Locate and identify every blood parasite.
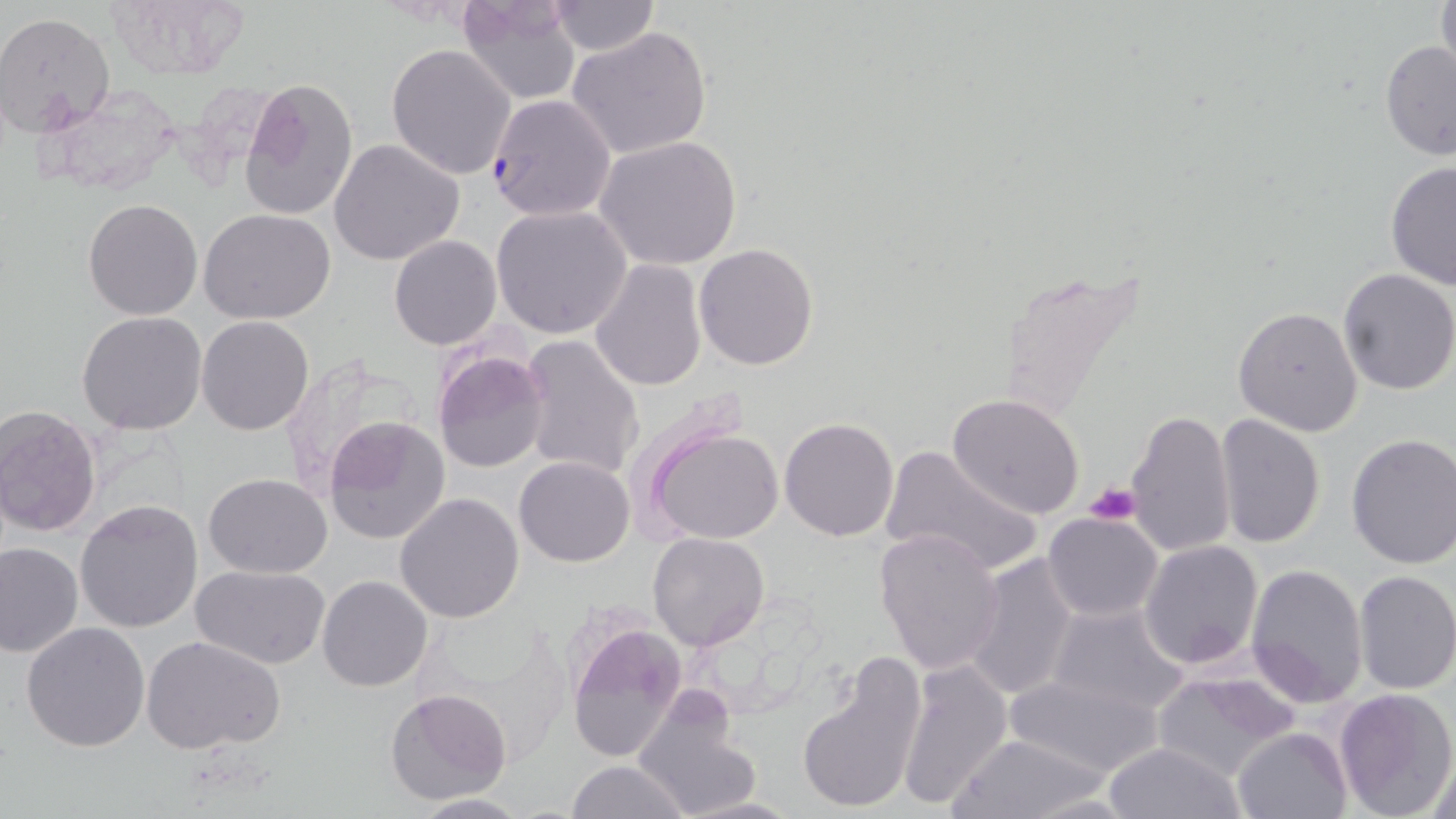
Approximate bounding boxes as named x1/y1/x2/y2 corners in pixels.
Plasmodium falciparum-infected red blood cells: (x1=486, y1=93, x2=617, y2=223).
No Plasmodium ovale, Plasmodium malariae, Plasmodium vivax, Babesia divergens, or Trypanosoma brucei observed.

Summary:
  - Platelet locations: (x1=1085, y1=483, x2=1142, y2=526)
  - Uninfected red blood cell locations: (x1=455, y1=0, x2=582, y2=105), (x1=1433, y1=0, x2=1455, y2=82), (x1=103, y1=1, x2=249, y2=81), (x1=547, y1=1, x2=660, y2=55), (x1=0, y1=13, x2=115, y2=137), (x1=567, y1=24, x2=714, y2=160), (x1=1379, y1=39, x2=1456, y2=160), (x1=386, y1=42, x2=516, y2=179), (x1=239, y1=75, x2=359, y2=223), (x1=594, y1=136, x2=743, y2=270), (x1=328, y1=139, x2=464, y2=267), (x1=1383, y1=159, x2=1456, y2=291), (x1=81, y1=199, x2=202, y2=320), (x1=489, y1=204, x2=632, y2=340), (x1=198, y1=209, x2=337, y2=325), (x1=389, y1=235, x2=501, y2=349), (x1=693, y1=243, x2=818, y2=370), (x1=591, y1=259, x2=708, y2=392), (x1=990, y1=267, x2=1153, y2=426), (x1=1336, y1=268, x2=1456, y2=395), (x1=1232, y1=306, x2=1364, y2=434), (x1=76, y1=311, x2=207, y2=434), (x1=196, y1=315, x2=315, y2=436), (x1=518, y1=334, x2=645, y2=481), (x1=432, y1=347, x2=550, y2=472), (x1=947, y1=394, x2=1086, y2=519), (x1=0, y1=406, x2=102, y2=539), (x1=1125, y1=409, x2=1236, y2=556), (x1=1214, y1=412, x2=1325, y2=550), (x1=323, y1=417, x2=451, y2=544), (x1=778, y1=418, x2=900, y2=541), (x1=645, y1=422, x2=786, y2=546), (x1=1345, y1=433, x2=1456, y2=569), (x1=879, y1=444, x2=1043, y2=580), (x1=514, y1=455, x2=634, y2=567), (x1=204, y1=473, x2=330, y2=577), (x1=394, y1=493, x2=523, y2=624), (x1=74, y1=498, x2=204, y2=633), (x1=1042, y1=511, x2=1163, y2=622), (x1=872, y1=528, x2=1005, y2=673), (x1=648, y1=532, x2=769, y2=651), (x1=1139, y1=540, x2=1262, y2=669), (x1=0, y1=542, x2=83, y2=659), (x1=963, y1=552, x2=1080, y2=701), (x1=192, y1=564, x2=331, y2=669), (x1=1244, y1=564, x2=1366, y2=708), (x1=1354, y1=570, x2=1456, y2=695), (x1=317, y1=575, x2=433, y2=692), (x1=1045, y1=600, x2=1191, y2=714), (x1=562, y1=619, x2=688, y2=765), (x1=22, y1=623, x2=151, y2=752), (x1=142, y1=636, x2=287, y2=754), (x1=795, y1=655, x2=926, y2=816), (x1=897, y1=659, x2=1012, y2=807), (x1=1004, y1=672, x2=1165, y2=777), (x1=1152, y1=672, x2=1300, y2=781), (x1=1334, y1=686, x2=1456, y2=818), (x1=385, y1=689, x2=511, y2=806), (x1=633, y1=696, x2=763, y2=818), (x1=1232, y1=727, x2=1351, y2=818), (x1=946, y1=733, x2=1112, y2=819), (x1=1101, y1=741, x2=1247, y2=819), (x1=1427, y1=748, x2=1455, y2=819), (x1=566, y1=760, x2=690, y2=819), (x1=407, y1=793, x2=530, y2=817), (x1=677, y1=794, x2=804, y2=818)
  - Slide-level diagnosis: Plasmodium falciparum
  - Image size: 1456×819 pixels
  - Field of view: single
  - Preparation: thin blood film
  - Magnification: 1000x
  - Stain: May-Grünwald-Giemsa
  - Modality: optical microscopy